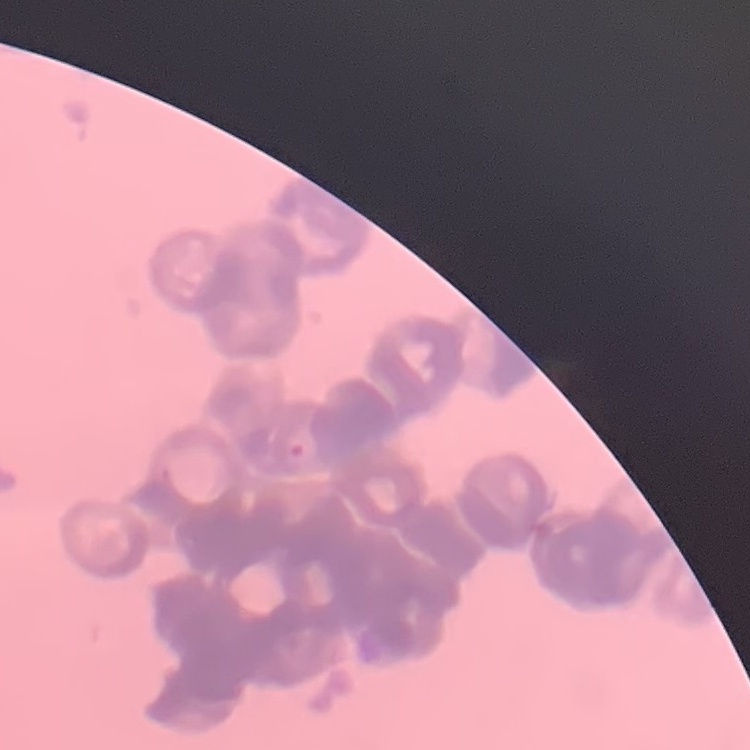

erythrocyte_morphology: rouleaux formation
stain: Field's or Giemsa
preparation: thin peripheral smear
image_type: one tile cut from a larger photomicrograph